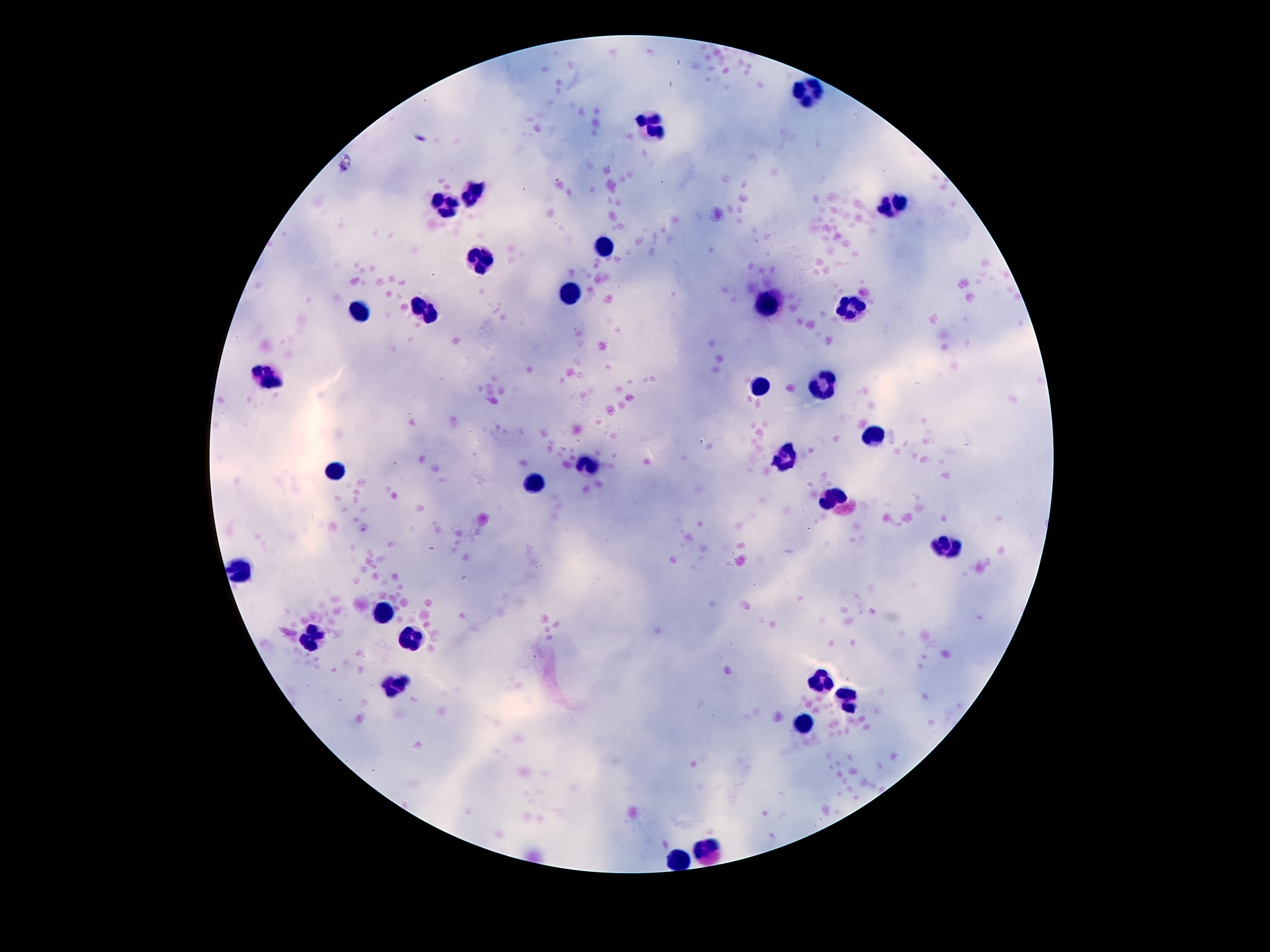 Approximate object centers, in pixels from the top-left corner. Leukocyte locations: (x=810, y=91), (x=651, y=128), (x=475, y=192), (x=444, y=205), (x=890, y=206), (x=604, y=246), (x=480, y=260), (x=574, y=294), (x=765, y=303), (x=851, y=309), (x=358, y=312), (x=426, y=312), (x=266, y=378), (x=821, y=385), (x=762, y=389), (x=874, y=432), (x=785, y=459), (x=587, y=464), (x=337, y=471), (x=534, y=485), (x=831, y=498), (x=946, y=548), (x=243, y=567), (x=384, y=612), (x=310, y=636), (x=416, y=641), (x=821, y=677), (x=393, y=684), (x=848, y=699), (x=806, y=722), (x=707, y=849), (x=676, y=858). Photographed through the microscope eyepiece with a smartphone camera. 100x magnification. Giemsa-stained preparation. Thick blood smear. One field from this slide. Image is 1270×952 pixels. Patient malaria status: not infected.